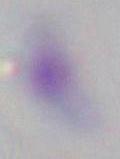
Summary:
  - Modality: micrograph
  - Identification: Toxoplasma gondii
  - Magnification: 1000x